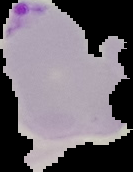 From a thin blood film. Malaria status: parasitized. Image is 133×172 pixels. The area outside the segmented cell region is set to black.